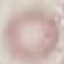 Result: no malaria parasites seen. Thin blood film. Photographed with a smartphone camera at the microscope eyepiece. Giemsa-stained preparation. Cell patch, automatically extracted from a larger field of view and resized to 64 × 64 pixels.